Classify this cell by malaria status.
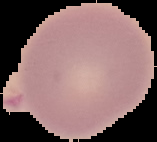

Uninfected.

Summary:
  - Image type: cell region segmented out of the field of view; surrounding area masked to black
  - Image size: 157×142 pixels
  - Preparation: thin blood film